State which parasite is depicted.
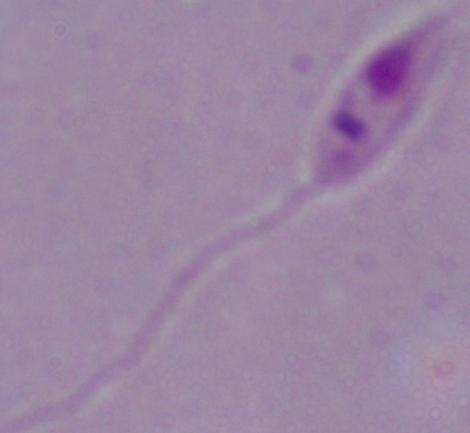

Leishmania.

Summary:
  - Modality: photomicrograph
  - Magnification: 1000x